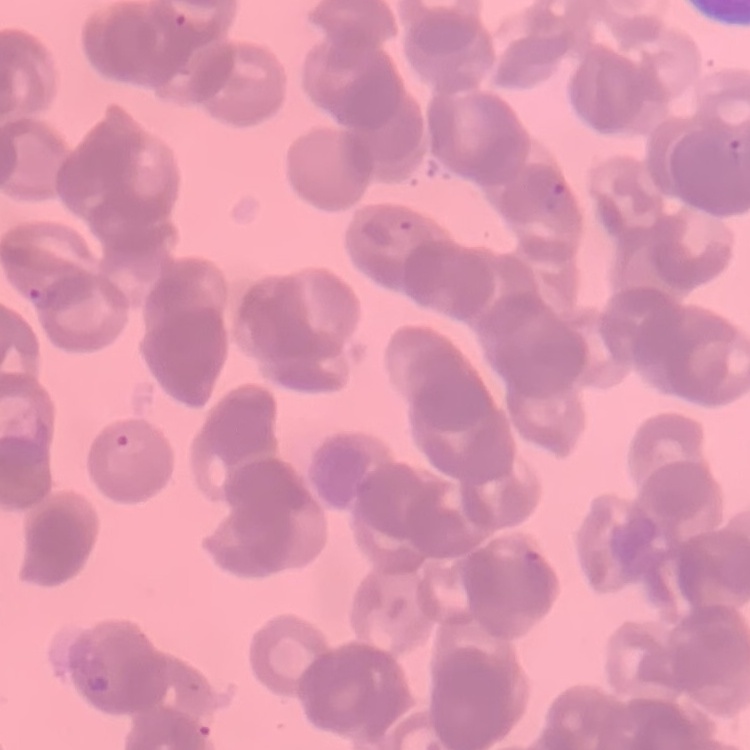
Summary:
  - Red blood cell morphology: rouleaux formation
  - Image type: one tile cut from a larger photomicrograph
  - Stain: Field's or Giemsa
  - Preparation: thin blood smear